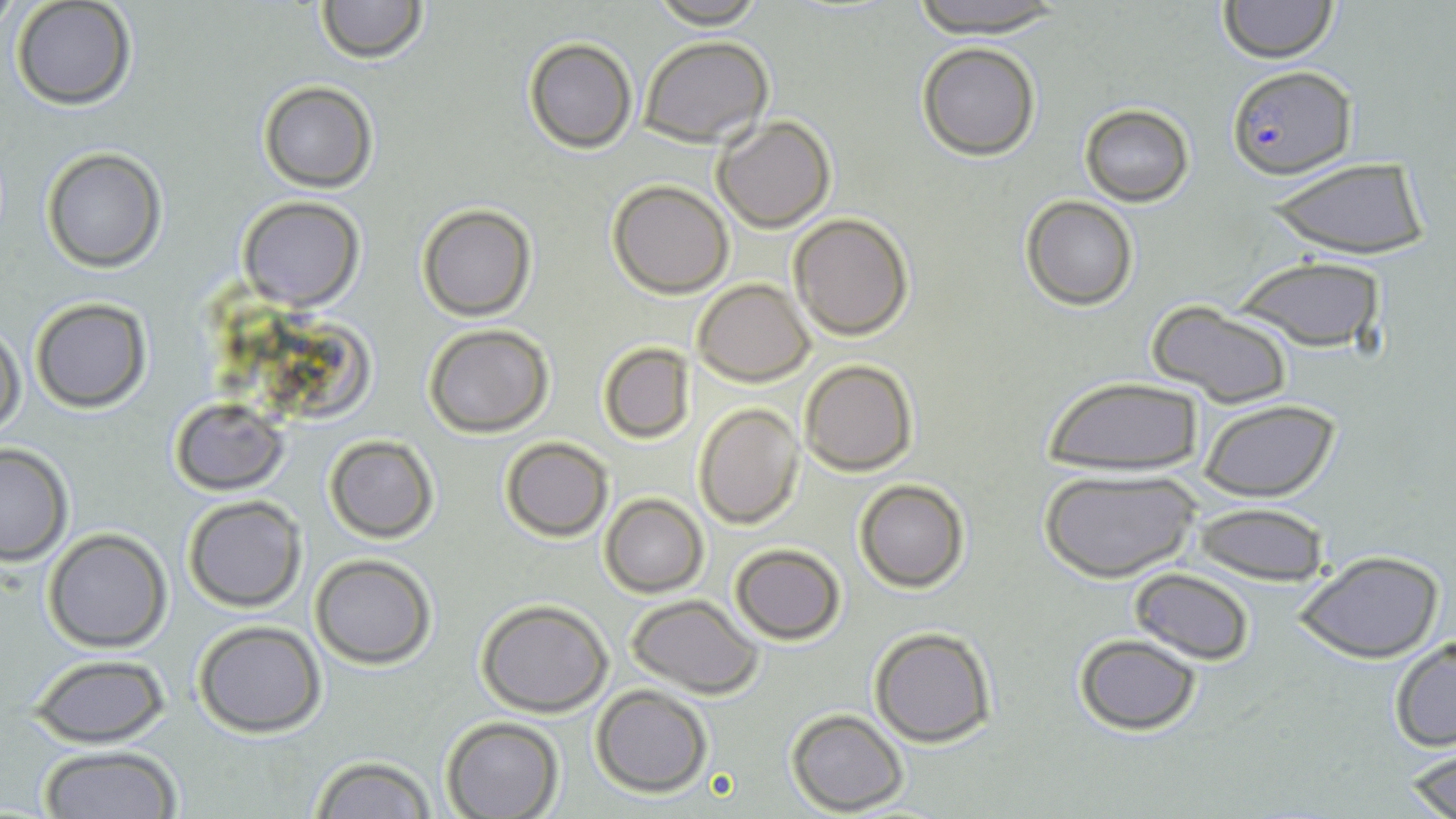 Approximate bounding boxes as named x1/y1/x2/y2 corners in pixels. Plasmodium falciparum-infected red blood cell locations: (x1=1226, y1=66, x2=1355, y2=180). Uninfected red blood cell locations: (x1=312, y1=0, x2=429, y2=64), (x1=645, y1=0, x2=770, y2=27), (x1=898, y1=0, x2=1078, y2=39), (x1=1217, y1=0, x2=1340, y2=62), (x1=12, y1=1, x2=137, y2=112), (x1=521, y1=35, x2=636, y2=154), (x1=639, y1=35, x2=773, y2=148), (x1=916, y1=42, x2=1041, y2=161), (x1=257, y1=80, x2=378, y2=192), (x1=1079, y1=104, x2=1194, y2=205), (x1=711, y1=114, x2=836, y2=231), (x1=41, y1=146, x2=166, y2=271), (x1=1265, y1=158, x2=1433, y2=261), (x1=606, y1=179, x2=734, y2=298), (x1=1020, y1=195, x2=1140, y2=311), (x1=235, y1=196, x2=364, y2=311), (x1=418, y1=203, x2=537, y2=320), (x1=787, y1=211, x2=914, y2=340), (x1=1230, y1=255, x2=1388, y2=354), (x1=693, y1=278, x2=815, y2=385), (x1=29, y1=297, x2=152, y2=413), (x1=1148, y1=302, x2=1294, y2=409), (x1=423, y1=323, x2=554, y2=437), (x1=0, y1=326, x2=26, y2=441), (x1=265, y1=329, x2=373, y2=423), (x1=597, y1=341, x2=695, y2=443), (x1=798, y1=358, x2=919, y2=476), (x1=1042, y1=376, x2=1206, y2=478), (x1=169, y1=397, x2=288, y2=494), (x1=1196, y1=397, x2=1343, y2=502), (x1=693, y1=403, x2=805, y2=529), (x1=323, y1=434, x2=440, y2=543), (x1=498, y1=435, x2=614, y2=542), (x1=0, y1=441, x2=76, y2=566), (x1=1037, y1=468, x2=1199, y2=585), (x1=853, y1=478, x2=970, y2=592), (x1=599, y1=494, x2=708, y2=597), (x1=182, y1=495, x2=306, y2=612), (x1=1190, y1=502, x2=1328, y2=586), (x1=43, y1=528, x2=172, y2=653), (x1=729, y1=543, x2=845, y2=644), (x1=1293, y1=548, x2=1445, y2=664), (x1=309, y1=554, x2=437, y2=669), (x1=1129, y1=567, x2=1256, y2=666), (x1=625, y1=594, x2=765, y2=698), (x1=475, y1=600, x2=614, y2=716), (x1=193, y1=620, x2=327, y2=738), (x1=869, y1=627, x2=997, y2=748), (x1=1072, y1=634, x2=1203, y2=734), (x1=1389, y1=634, x2=1456, y2=753), (x1=26, y1=654, x2=173, y2=748), (x1=591, y1=685, x2=715, y2=797), (x1=784, y1=709, x2=909, y2=814), (x1=440, y1=716, x2=564, y2=819), (x1=1402, y1=741, x2=1456, y2=819), (x1=34, y1=745, x2=183, y2=819), (x1=309, y1=756, x2=440, y2=818). Slide-level diagnosis: Plasmodium falciparum. Light microscopy. Image is 1456×819 pixels. Thin blood smear. Single field of view. May-Grünwald-Giemsa-stained preparation. Captured at 1000x magnification.